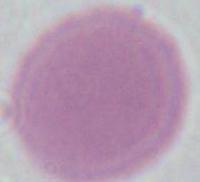
Photomicrograph. An erythrocyte is shown. 1000x magnification.